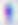
Summary:
  - Modality: photomicrograph
  - Identification: Toxoplasma gondii
  - Magnification: 400x